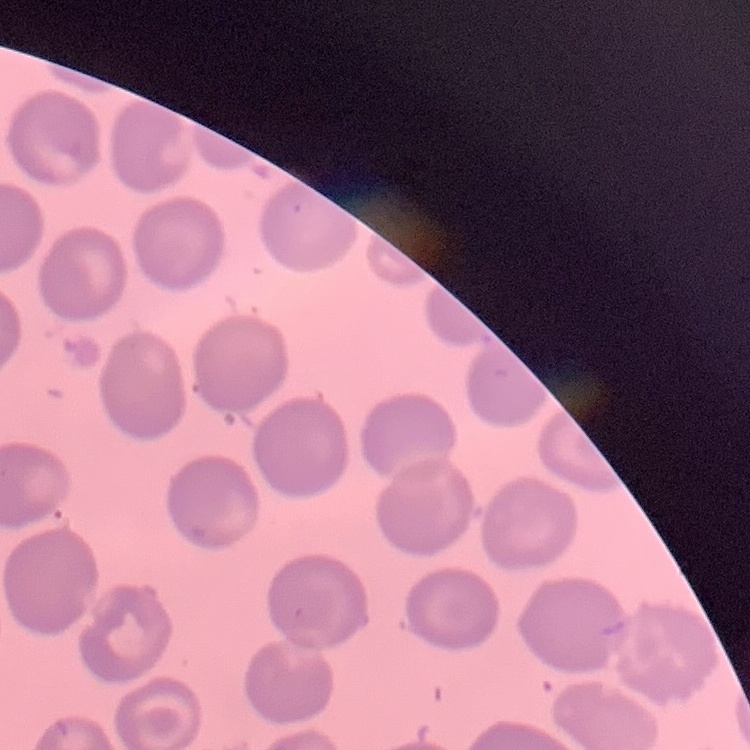

erythrocyte morphology = no rouleaux formation
image type = square crop of a larger photomicrograph
preparation = thin peripheral smear
stain = Field's or Giemsa